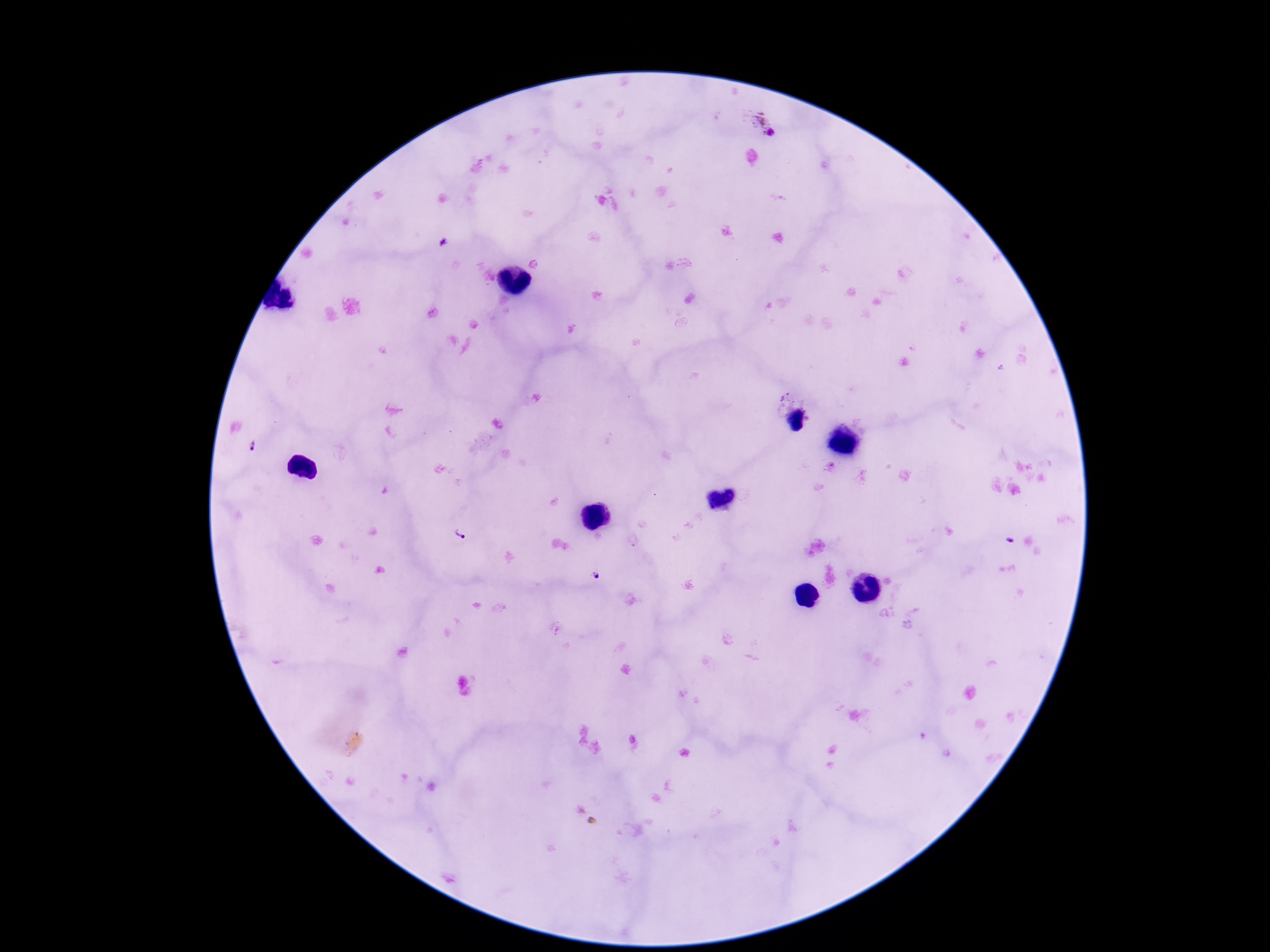

Approximate centers as {x, y} in pixels.
Summary:
  - Plasmodium parasite locations: {759, 124}, {249, 446}, {459, 533}, {595, 576}
  - Patient malaria status: infected
  - Field of view: single
  - Magnification: 100x
  - Stain: Giemsa
  - Preparation: thick blood smear
  - Image size: 1270×952 pixels
  - Capture: smartphone camera through the microscope eyepiece